Locate every Plasmodium parasite.
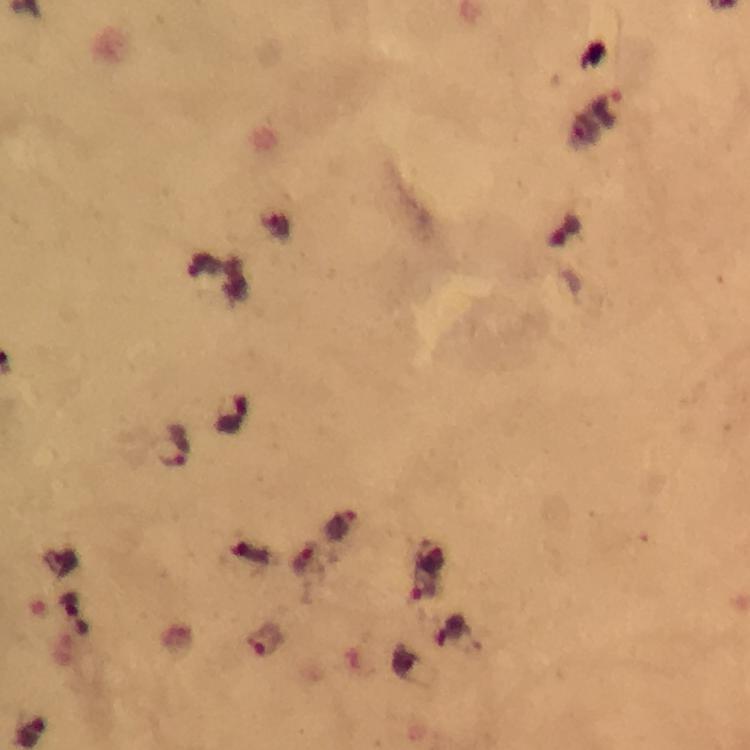

Approximate centers as {x, y} in pixels.
Plasmodium parasites: {610, 107}, {175, 447}, {338, 525}, {424, 579}, {268, 639}.

Summary:
  - Preparation: thick smear
  - Image size: 750×750 pixels
  - Cropped from: a single field of view
  - Capture: smartphone mounted on the microscope
  - Immersion oil: used
  - Magnification: 100x
  - Stain: Giemsa
  - Context: from a diagnostic examination for malaria